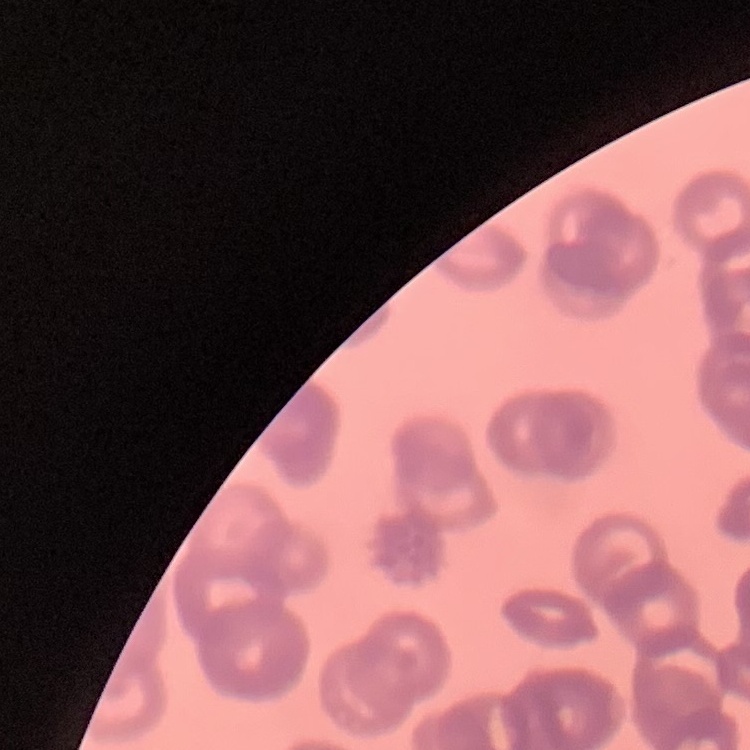
The red blood cells exhibit rouleaux formation. Stained with either Field's or Giemsa. Thin blood smear. Square crop of a larger photomicrograph.